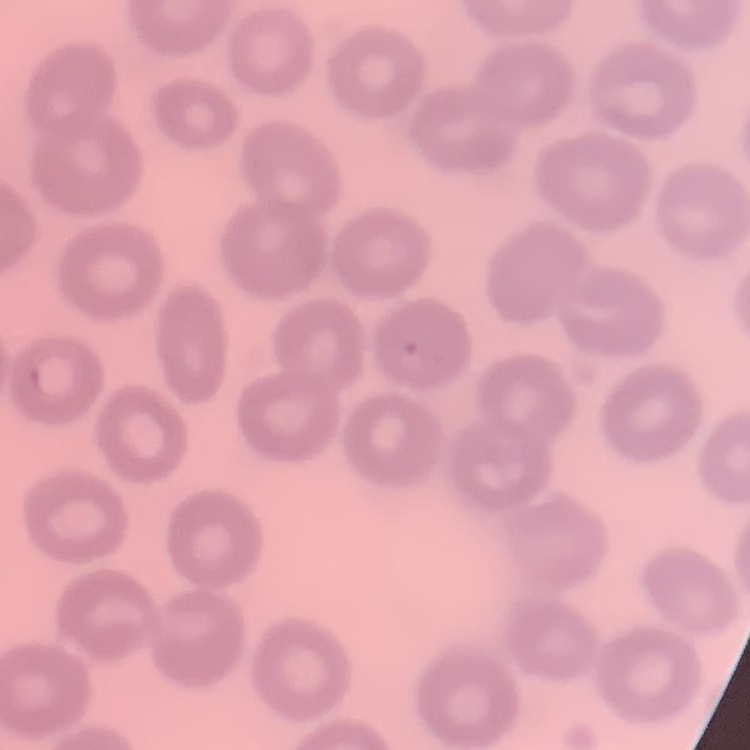

erythrocyte_morphology: no rouleaux formation
image_type: one tile cut from a larger photomicrograph
stain: Field's or Giemsa
preparation: thin peripheral smear